Find the cells and give the type of each one.
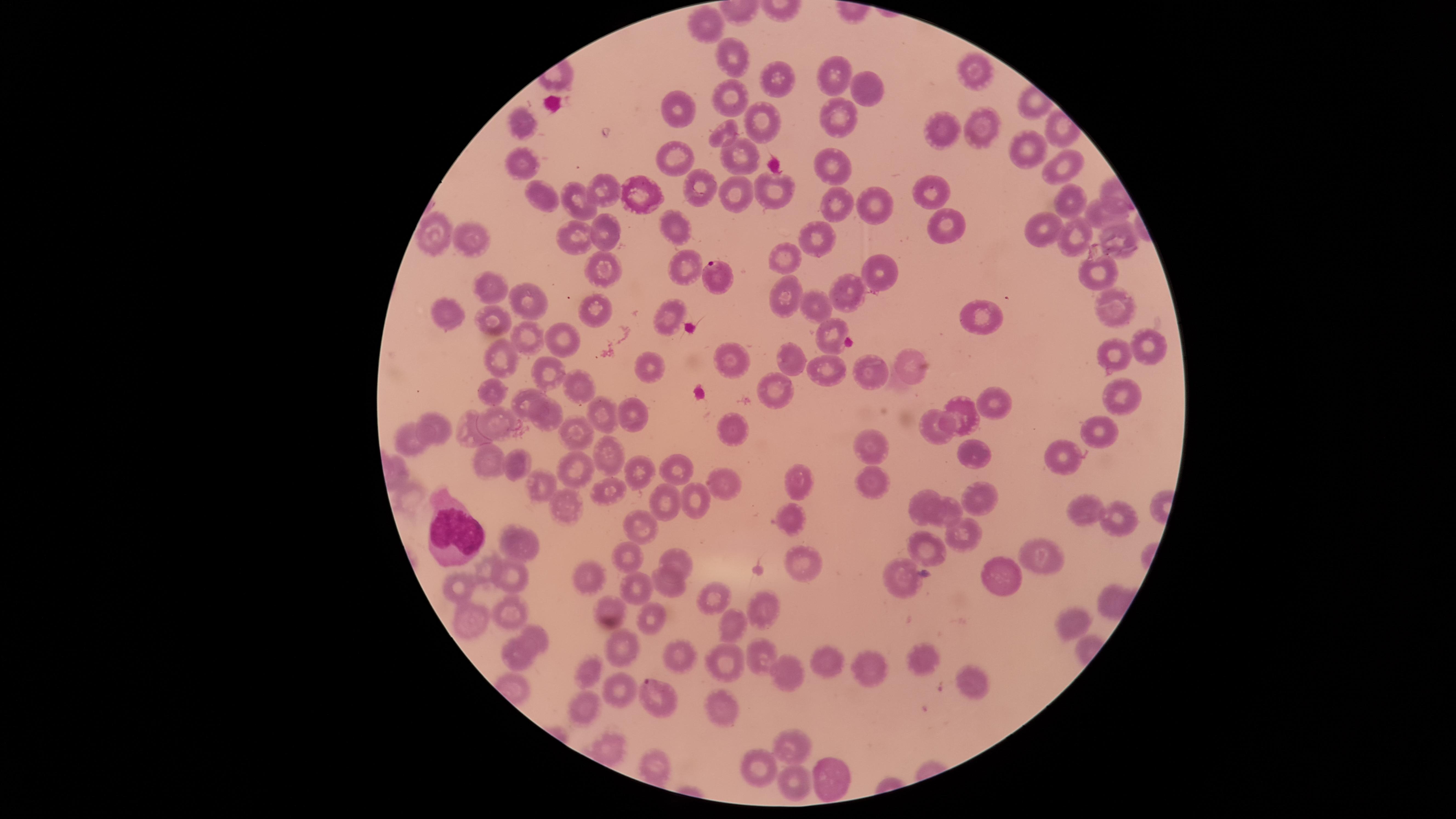

Approximate marker points as (x, y) in pixels.
Parasitized red blood cells: (716, 275), (660, 698).
Uninfected red blood cells: (703, 20), (735, 57), (978, 64), (828, 73), (774, 82), (869, 93), (727, 97), (682, 100), (841, 111), (519, 123), (763, 123), (979, 125), (942, 130), (720, 135), (1020, 147), (735, 157), (525, 160), (677, 160), (828, 162), (1072, 164), (697, 185), (605, 189), (928, 189), (772, 190), (639, 194), (544, 195), (728, 196), (1066, 198), (582, 200), (868, 201), (839, 204), (1099, 212), (942, 218), (1036, 229), (1114, 231), (606, 232), (812, 233), (1071, 233), (433, 234), (674, 234), (467, 237), (576, 237), (786, 253), (603, 265), (684, 268), (879, 271), (1095, 273), (493, 291), (847, 293), (786, 295), (526, 300), (815, 302), (1116, 305), (442, 310), (598, 312), (669, 315), (979, 315), (494, 321), (830, 333), (528, 337), (558, 337), (1149, 345), (729, 355), (786, 355), (1109, 355), (499, 357), (647, 365), (916, 365), (832, 369), (550, 372), (873, 372), (571, 381), (773, 388), (498, 394), (1128, 395), (533, 398), (991, 405), (602, 410), (962, 410), (628, 411), (493, 416), (548, 421), (934, 427), (440, 428), (1100, 428), (731, 429), (579, 431), (472, 432), (411, 438), (871, 441), (604, 454), (971, 454), (1060, 458), (492, 461), (521, 468), (571, 468), (635, 470), (680, 471), (801, 475), (875, 479), (723, 483), (537, 485), (606, 494), (985, 496), (665, 502), (692, 502), (926, 502), (569, 508), (948, 510), (1083, 511), (1122, 514), (792, 516), (640, 531), (962, 538), (521, 543), (928, 544), (1035, 549), (626, 553), (678, 558), (487, 562), (806, 562), (900, 571), (997, 573), (514, 575), (590, 575), (670, 582), (458, 584), (637, 585), (712, 593), (607, 602), (762, 604), (510, 612), (467, 620), (652, 620), (1065, 620), (732, 625), (538, 634), (623, 641), (679, 649), (755, 655), (520, 658), (921, 658), (827, 659), (722, 662), (868, 668), (585, 671), (781, 674), (615, 685), (976, 686), (590, 701), (726, 713), (611, 744), (793, 744), (759, 770), (826, 772), (796, 779).
White blood cells: (454, 533).

Giemsa-stained preparation. Single field of view. Thin blood smear. Species: Plasmodium falciparum. Image is 1456×819 pixels. Circular visible region. Photographed with a smartphone camera through the microscope eyepiece.